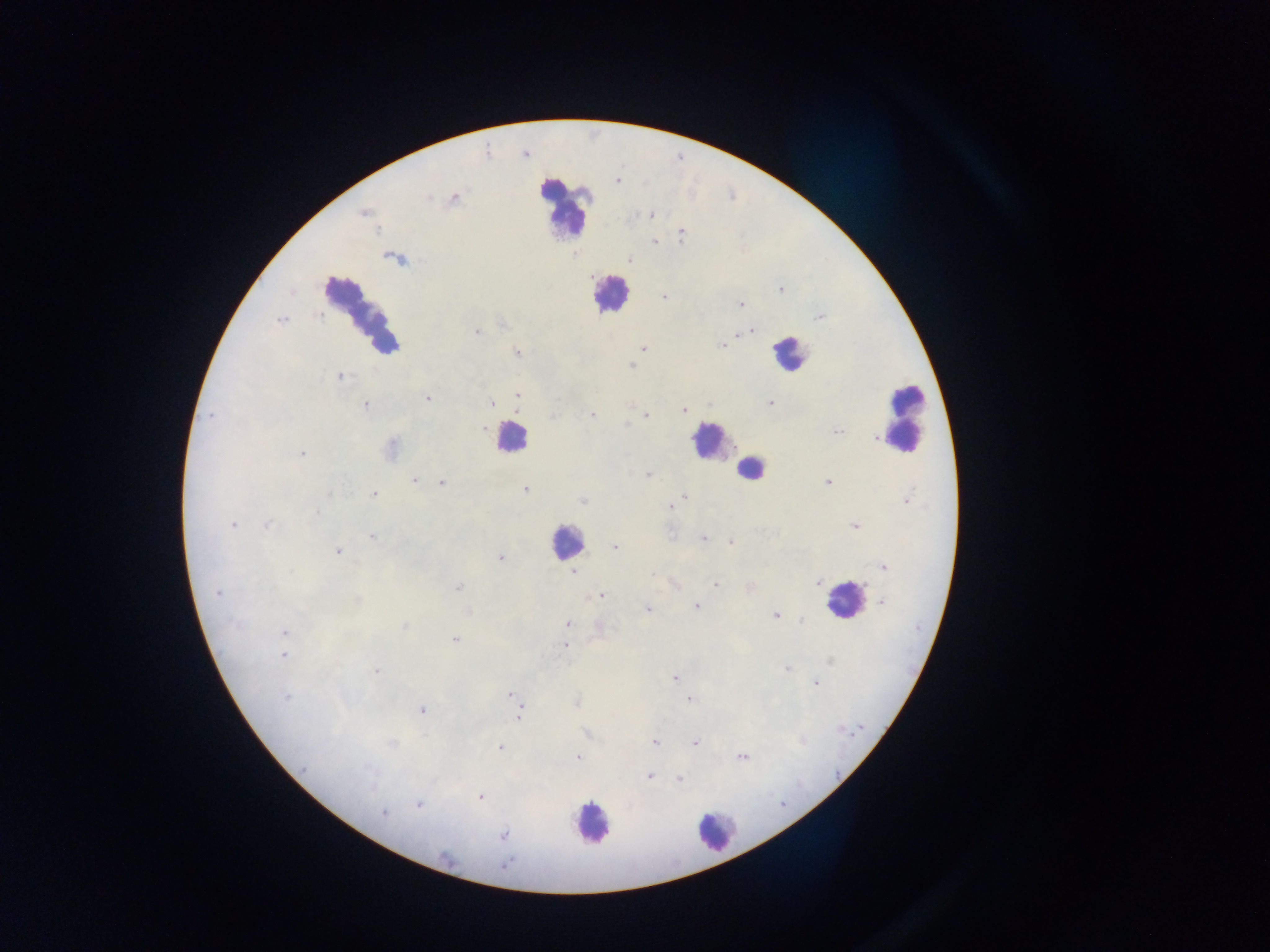
image size = 1270×952 pixels
capture = mobile-phone photograph through a microscope
malaria parasite locations = approximate centers as {x, y} in pixels: {618, 181}, {428, 198}, {455, 198}, {363, 213}, {651, 215}, {681, 233}, {654, 241}, {629, 260}, {780, 289}, {664, 296}, {741, 304}, {820, 317}, {281, 320}, {476, 331}, {752, 331}, {740, 334}, {723, 346}, {643, 349}, {517, 352}, {632, 365}, {340, 376}, {517, 396}, {428, 398}, {770, 402}, {491, 404}, {365, 406}, {684, 410}, {211, 415}, {592, 415}, {646, 415}, {483, 429}, {839, 431}, {874, 438}, {302, 453}, {647, 475}, {413, 481}, {441, 483}, {828, 483}, {525, 490}, {373, 494}, {684, 495}, {907, 500}, {583, 501}, {669, 508}, {316, 514}, {232, 524}, {267, 525}, {854, 526}, {371, 537}, {703, 539}, {731, 542}, {614, 547}, {338, 552}, {500, 557}, {884, 567}, {573, 572}, {653, 574}, {818, 583}, {716, 585}, {458, 587}, {218, 593}, {601, 596}, {357, 600}, {881, 602}, {696, 606}, {647, 609}, {775, 615}, {802, 620}, {567, 623}, {234, 624}, {405, 626}, {283, 632}, {455, 640}, {565, 645}, {283, 654}, {787, 668}, {376, 671}, {674, 679}, {815, 683}, {510, 695}, {286, 698}, {690, 700}, {575, 702}, {423, 710}, {519, 714}, {655, 743}, {695, 743}, {392, 745}, {500, 747}, {577, 757}, {742, 757}, {368, 768}, {304, 769}, {649, 777}, {679, 779}, {480, 797}, {418, 805}, {383, 813}, {503, 834}, {505, 864}
field of view = single
preparation = thick blood film
leukocyte locations = approximate centers as {x, y} in pixels: {565, 206}, {609, 294}, {359, 309}, {789, 352}, {905, 417}, {510, 437}, {710, 441}, {750, 470}, {566, 541}, {843, 599}, {591, 824}, {716, 832}
country = Ghana